Classify this cell by malaria status.
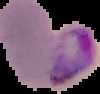

It is parasitized.

Summary:
  - Image size: 100×94 pixels
  - Image type: segmented cell region on a black background
  - Preparation: thin blood smear